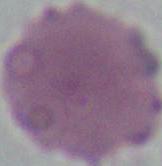

Photomicrograph. 1000x magnification. An erythrocyte is shown.